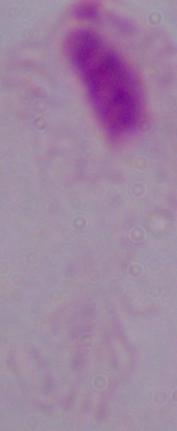
Summary:
  - Magnification: 1000x
  - Modality: micrograph
  - Identification: trichomonad